Identify the parasite.
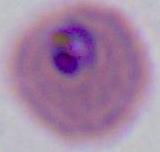

Plasmodium.

Summary:
  - Magnification: 400x or 1000x
  - Modality: micrograph